Give the position of every Plasmodium parasite visible.
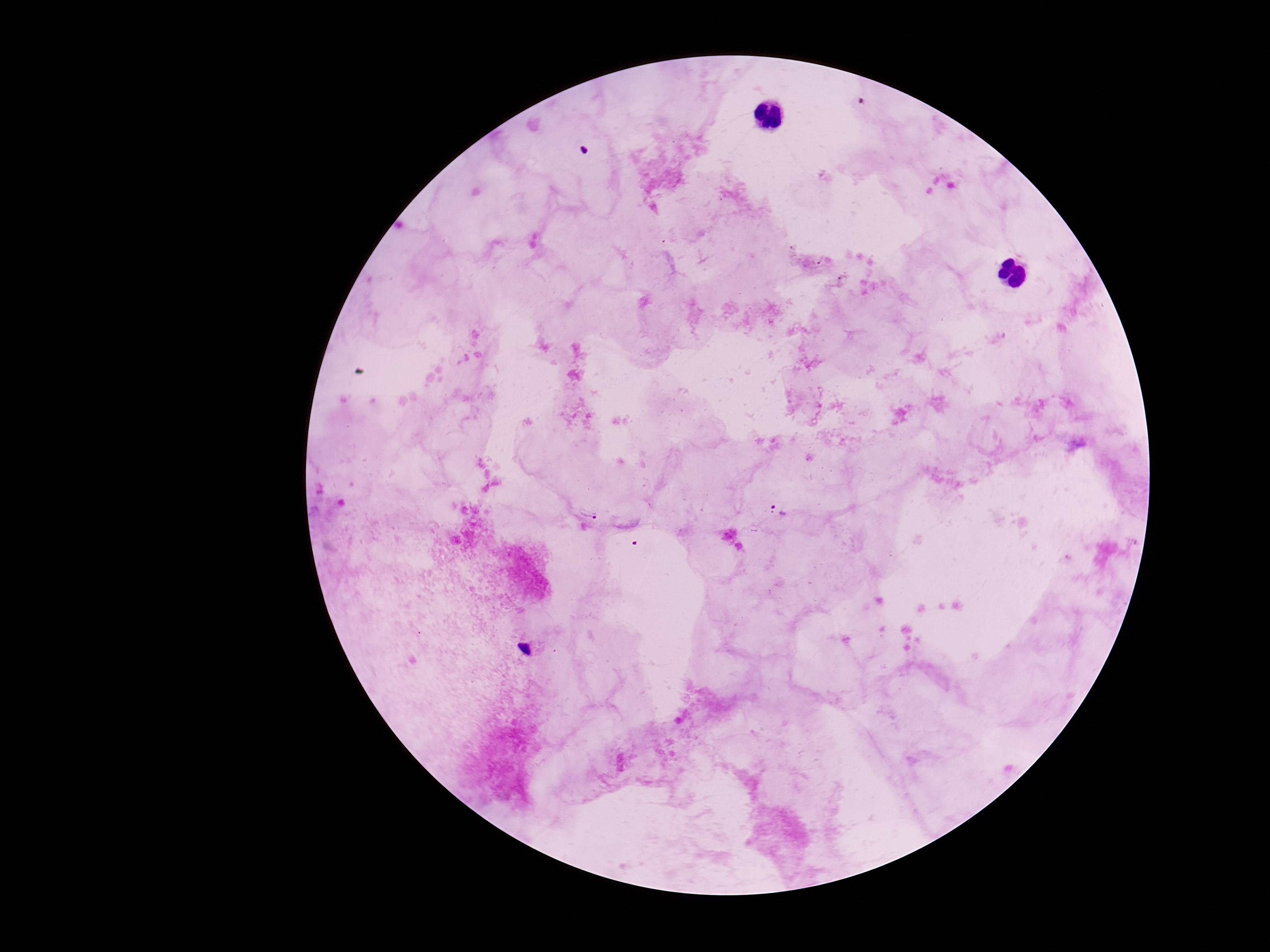

Approximate centers as (x, y) in pixels.
Plasmodium parasites: (780, 511).

{
  "preparation": "thick peripheral-blood smear",
  "magnification": "100x",
  "patient_malaria_status": "positive",
  "field_of_view": "one from this slide",
  "capture": "smartphone camera through the microscope eyepiece",
  "image_size": "1270×952 pixels",
  "stain": "Giemsa"
}